Locate every blood parasite and identify its species.
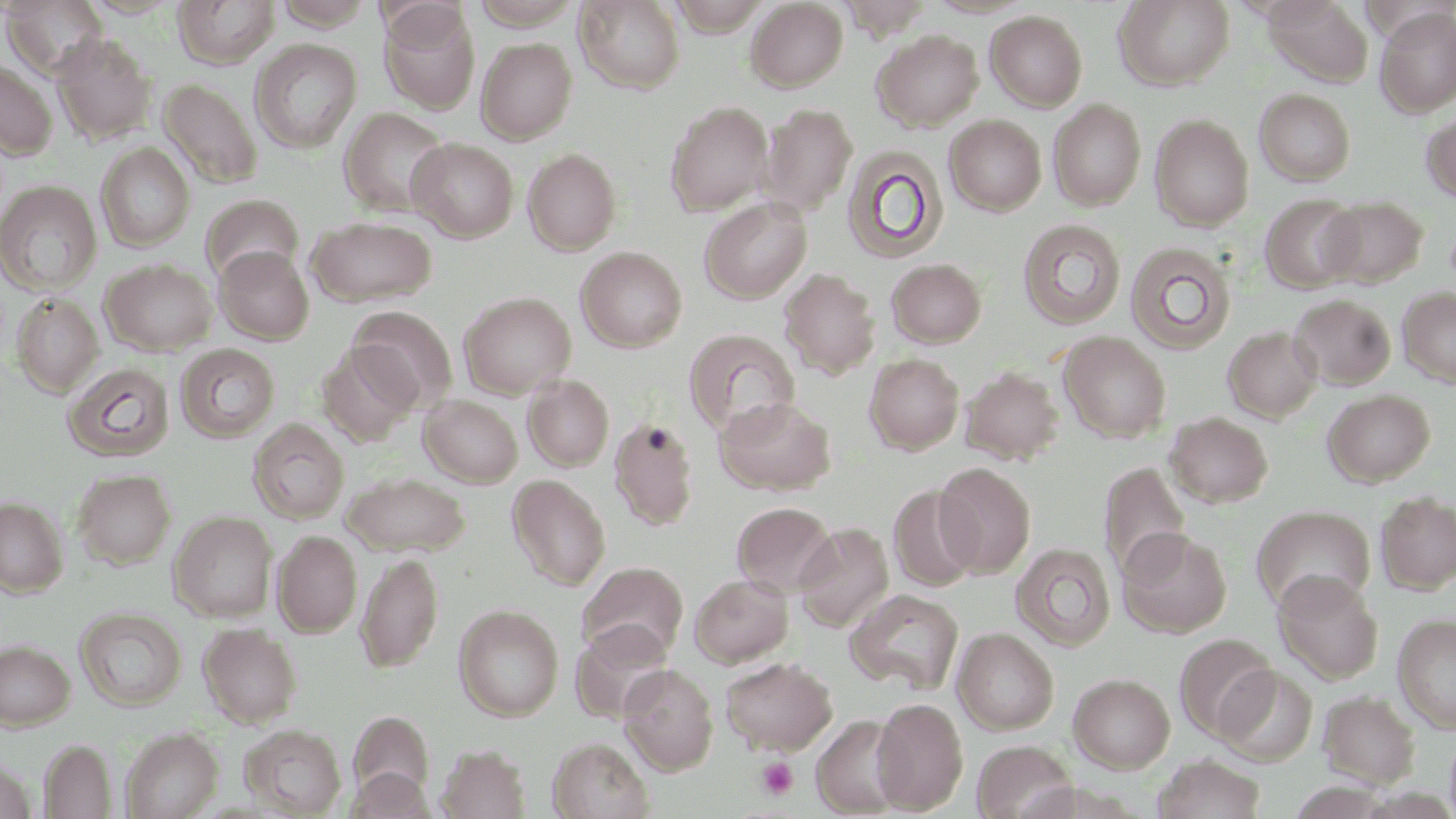
No blood parasites seen.

Approximate bounding boxes as [x1, y1, x2, y2] in pixels. Platelet locations: [756, 756, 799, 800]. Uninfected red blood cell locations: [1, 0, 110, 80], [79, 0, 185, 18], [173, 0, 280, 69], [472, 0, 581, 29], [574, 0, 685, 93], [667, 0, 773, 35], [745, 0, 849, 92], [839, 0, 935, 39], [1114, 0, 1235, 90], [1263, 0, 1373, 87], [378, 3, 480, 114], [1375, 8, 1456, 117], [984, 10, 1088, 112], [872, 29, 983, 131], [53, 33, 157, 145], [476, 37, 577, 144], [250, 38, 362, 153], [0, 60, 58, 160], [158, 78, 263, 188], [1254, 88, 1356, 186], [1048, 98, 1146, 212], [664, 100, 774, 217], [759, 104, 857, 217], [339, 107, 451, 217], [1421, 112, 1456, 203], [945, 114, 1047, 216], [1150, 114, 1254, 231], [407, 138, 518, 242], [95, 142, 195, 253], [842, 145, 949, 265], [522, 148, 621, 255], [0, 180, 102, 295], [200, 194, 304, 284], [1260, 194, 1362, 293], [699, 196, 812, 304], [1319, 196, 1427, 289], [307, 216, 438, 307], [1017, 219, 1126, 330], [1017, 232, 1236, 338], [1125, 241, 1237, 355], [214, 245, 314, 344], [575, 246, 687, 352], [886, 258, 987, 348], [100, 259, 217, 356], [780, 268, 880, 379], [1398, 286, 1456, 388], [458, 291, 577, 399], [11, 293, 104, 397], [1289, 294, 1396, 391], [348, 305, 459, 411], [1223, 326, 1323, 422], [683, 329, 801, 437], [1058, 331, 1172, 442], [316, 342, 422, 446], [174, 343, 280, 442], [864, 353, 965, 454], [63, 362, 175, 462], [960, 365, 1064, 466], [523, 374, 614, 472], [1323, 389, 1435, 486], [419, 395, 523, 487], [715, 395, 836, 495], [1165, 412, 1274, 508], [609, 417, 699, 530], [247, 418, 349, 523], [1099, 461, 1191, 582], [933, 462, 1036, 578], [72, 469, 176, 570], [342, 472, 471, 557], [508, 474, 610, 591], [888, 485, 982, 591], [1375, 491, 1456, 595], [1, 497, 67, 596], [732, 502, 837, 596], [1251, 505, 1376, 615], [169, 511, 277, 622], [794, 522, 894, 633], [1118, 529, 1232, 637], [273, 530, 362, 637], [1011, 543, 1116, 651], [355, 553, 443, 673], [578, 561, 689, 663], [1273, 571, 1383, 685], [689, 573, 794, 667], [846, 588, 964, 695], [454, 604, 564, 721], [75, 606, 187, 711], [1392, 613, 1456, 733], [571, 620, 675, 723], [198, 622, 302, 728], [952, 628, 1059, 734], [1174, 632, 1278, 741], [0, 641, 75, 729], [719, 656, 837, 754], [619, 664, 719, 775], [1216, 665, 1319, 767], [1068, 672, 1175, 773], [1318, 690, 1420, 787], [871, 697, 968, 813], [348, 711, 435, 803], [811, 714, 911, 817], [240, 724, 346, 817], [120, 727, 223, 819], [1444, 727, 1456, 819], [547, 738, 653, 819], [39, 739, 117, 818], [972, 740, 1076, 819], [437, 744, 531, 819], [1152, 755, 1267, 818], [347, 768, 434, 818]. Slide-level diagnosis: no evidence of blood parasites. One field of a larger specimen. Captured at 1000x magnification. Light microscopy. May-Grünwald-Giemsa-stained preparation. Thin blood film. Image is 1456×819 pixels.